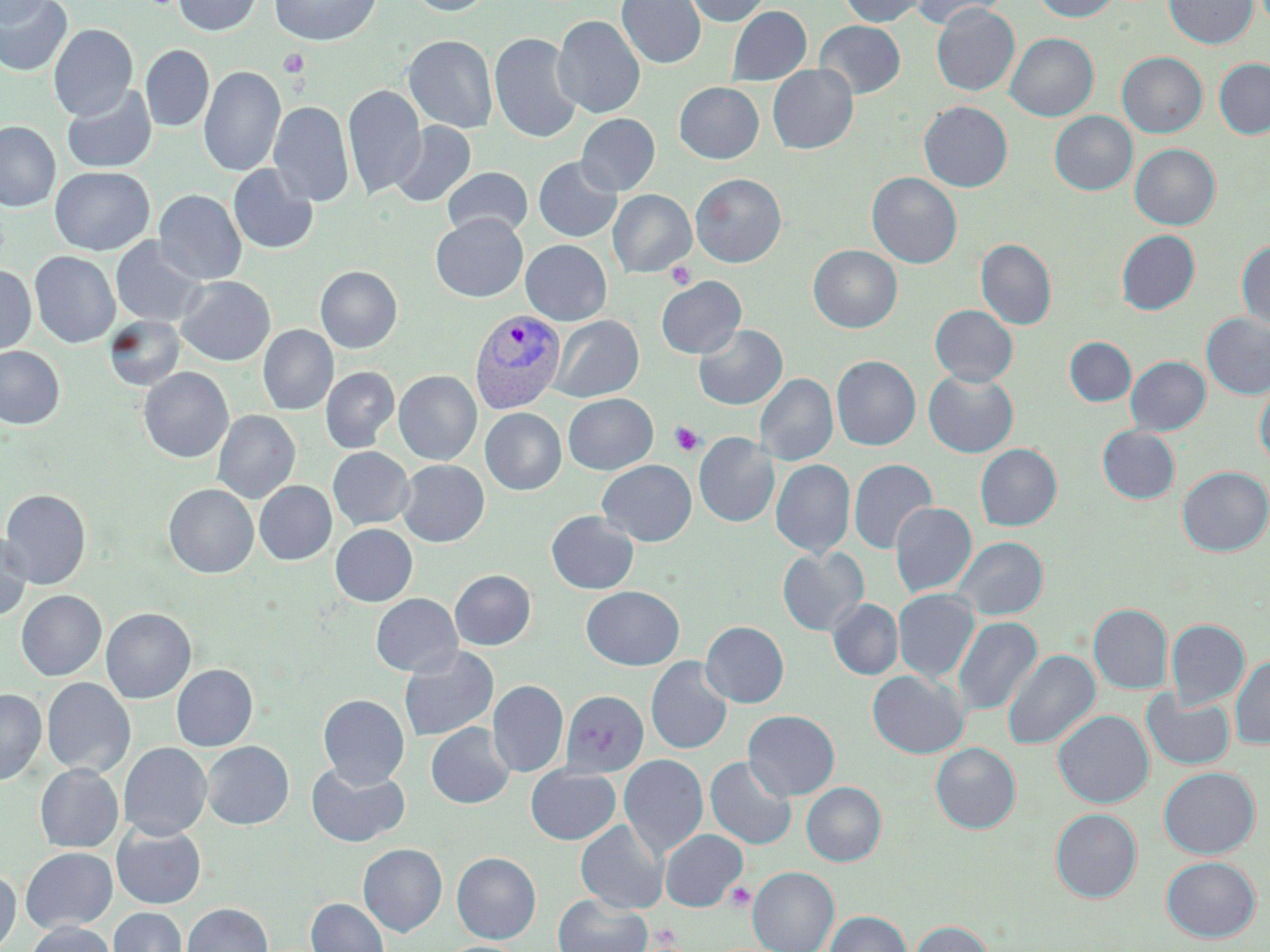

Approximate bounding boxes as [x1, y1, x2, y2] in pixels. Uninfected red blood cell locations: [0, 0, 73, 76], [0, 0, 49, 29], [172, 0, 262, 36], [269, 0, 382, 46], [405, 0, 496, 16], [616, 0, 706, 69], [682, 0, 773, 26], [838, 0, 928, 27], [912, 0, 1006, 30], [1031, 0, 1121, 22], [1163, 0, 1258, 49], [931, 3, 1020, 96], [727, 6, 811, 85], [552, 15, 645, 118], [814, 20, 906, 99], [48, 24, 138, 121], [489, 32, 582, 144], [1005, 33, 1099, 122], [402, 35, 498, 134], [141, 45, 214, 131], [1117, 52, 1207, 138], [1214, 58, 1270, 139], [767, 64, 858, 154], [199, 65, 286, 177], [674, 82, 764, 164], [343, 84, 425, 200], [62, 85, 158, 173], [268, 100, 353, 207], [918, 101, 1013, 192], [1050, 111, 1137, 196], [576, 113, 660, 196], [0, 121, 60, 212], [390, 121, 476, 208], [1130, 144, 1220, 230], [533, 157, 622, 242], [227, 164, 319, 255], [50, 166, 154, 255], [442, 167, 532, 239], [867, 172, 962, 269], [691, 173, 786, 267], [154, 190, 246, 285], [608, 190, 696, 278], [431, 214, 528, 302], [1117, 230, 1200, 315], [110, 236, 207, 327], [976, 239, 1056, 330], [521, 240, 612, 326], [1237, 240, 1270, 331], [808, 244, 902, 333], [29, 251, 120, 348], [0, 266, 36, 354], [315, 266, 402, 353], [176, 276, 275, 366], [656, 276, 746, 359], [930, 305, 1017, 386], [1201, 313, 1270, 399], [104, 315, 186, 391], [548, 315, 643, 402], [693, 324, 787, 410], [258, 325, 338, 415], [1065, 337, 1136, 406], [0, 346, 65, 429], [831, 355, 920, 450], [1126, 356, 1210, 435], [138, 367, 233, 463], [320, 367, 399, 452], [394, 370, 481, 464], [923, 370, 1019, 457], [755, 373, 838, 466], [1255, 380, 1270, 469], [563, 393, 658, 474], [480, 408, 566, 495], [212, 410, 300, 504], [1098, 426, 1179, 503], [694, 432, 779, 528], [975, 443, 1062, 531], [328, 447, 414, 529], [597, 459, 696, 546], [771, 459, 855, 558], [848, 459, 937, 554], [396, 460, 489, 547], [1177, 466, 1270, 556], [254, 481, 336, 565], [164, 484, 258, 578], [0, 489, 91, 589], [890, 502, 977, 598], [546, 511, 639, 594], [330, 524, 417, 606], [0, 530, 32, 621], [953, 537, 1048, 620], [777, 547, 868, 636], [450, 569, 536, 650], [581, 586, 684, 670], [893, 589, 979, 683], [16, 590, 106, 681], [370, 593, 461, 677], [828, 598, 903, 680], [1089, 604, 1173, 694], [101, 608, 196, 703], [953, 616, 1042, 717], [1166, 619, 1250, 709], [701, 621, 789, 707], [398, 646, 499, 742], [1002, 649, 1100, 752], [1230, 655, 1270, 750], [645, 657, 733, 754], [171, 664, 257, 751], [867, 670, 968, 758], [42, 678, 135, 778], [488, 680, 568, 777], [0, 688, 46, 785], [561, 690, 650, 776], [1141, 691, 1236, 770], [318, 694, 409, 787], [743, 710, 840, 800], [1053, 710, 1153, 808], [426, 723, 515, 808], [202, 741, 293, 829], [118, 743, 211, 840], [931, 743, 1020, 833], [619, 754, 708, 858], [705, 756, 797, 850], [306, 762, 410, 847], [35, 764, 123, 853], [526, 766, 621, 844], [1159, 767, 1260, 858], [801, 782, 886, 866], [1051, 808, 1142, 902], [576, 819, 668, 913], [111, 824, 206, 908], [660, 829, 747, 911], [358, 843, 447, 936], [20, 847, 117, 933], [452, 852, 541, 943], [1161, 856, 1260, 942], [748, 866, 839, 952], [0, 869, 20, 952], [553, 894, 653, 952], [306, 898, 389, 952], [181, 903, 273, 952], [109, 907, 187, 952], [826, 910, 912, 952], [911, 920, 993, 952], [24, 922, 117, 952]. Platelet locations: [277, 49, 309, 79], [665, 261, 696, 289], [669, 421, 704, 456], [725, 883, 755, 912]. Plasmodium vivax-infected red blood cell locations: [470, 309, 566, 414]. Slide-level diagnosis: Plasmodium vivax. Single field of view. May-Grünwald-Giemsa stain. Thin blood smear. Light microscopy. Image is 1270×952 pixels. 1000x magnification.